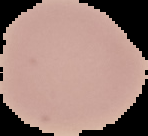

result = no Plasmodium parasites detected
preparation = thin blood film
image size = 148×136 pixels
image type = segmented cell region on a black background